Classify this cell by malaria status.
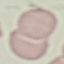
It is uninfected.

capture = smartphone camera at the microscope eyepiece
stain = Giemsa
preparation = thin blood smear
image type = automatically extracted cell patch, resized to 64 × 64 pixels